Name the cell type shown.
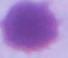

An erythrocyte.

modality = photomicrograph
magnification = 1000x